Assess this cell for malaria.
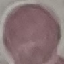
Uninfected.

capture: smartphone through the microscope eyepiece
image_type: cell patch, automatically extracted from a larger field of view and resized to 64 × 64 pixels
stain: Giemsa
preparation: thin smear